Give the preparation type.
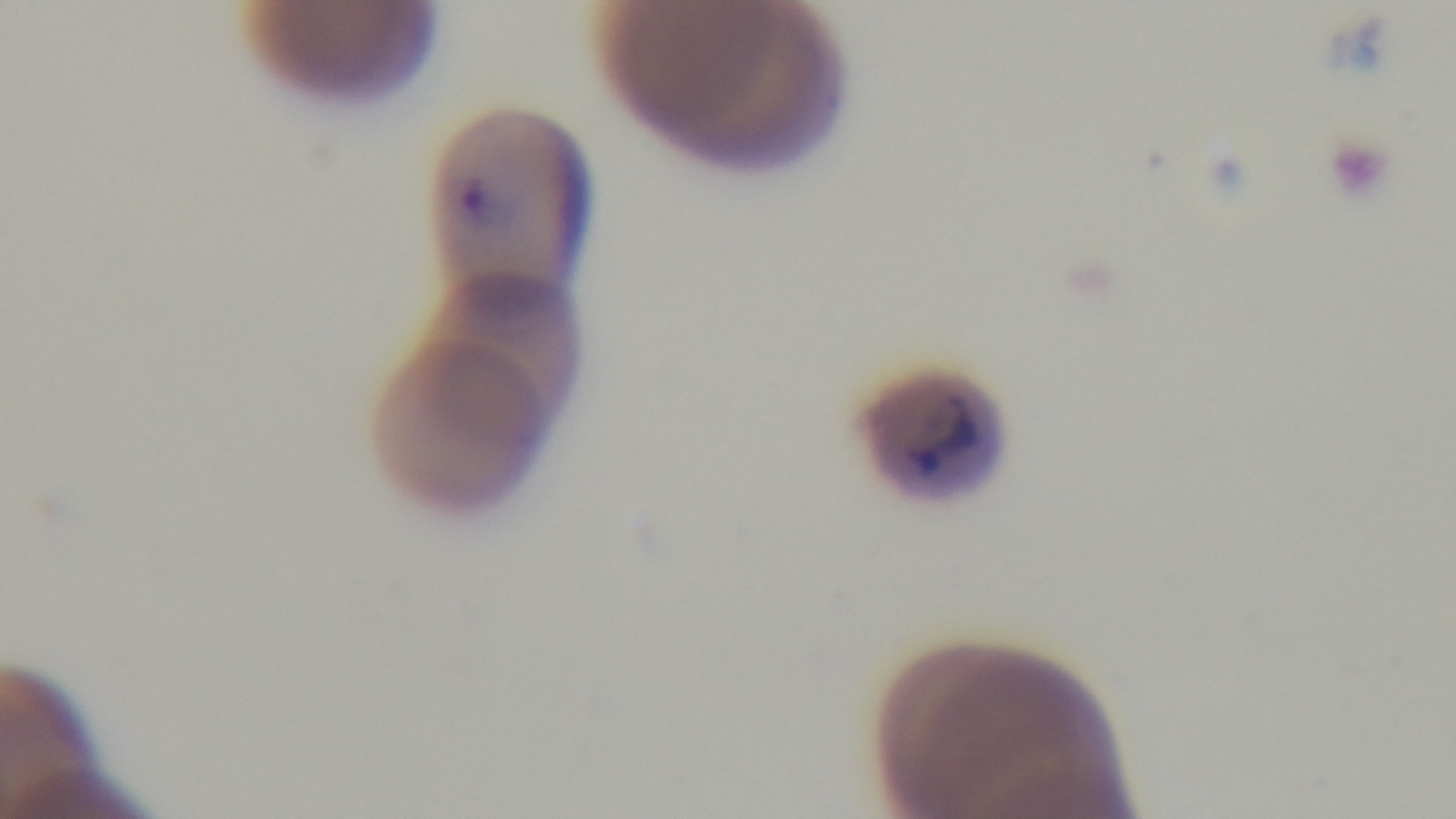

It is a thin blood film.

Mounted 4K digital camera. Oil-immersion objective, 100x. Giemsa-stained. Single field of view. Light microscopy. Malaria status: positive.